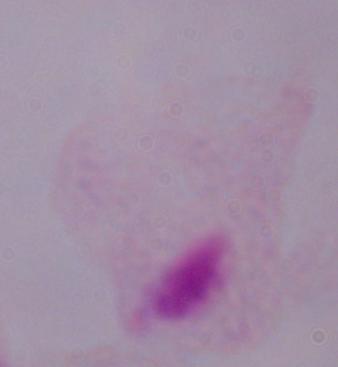

identification = trichomonad
modality = micrograph
magnification = 1000x